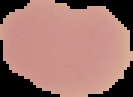

The area outside the segmented cell region is set to black. Malaria status: uninfected. From a thin blood smear. Image is 133×97 pixels.